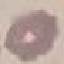
Result: negative for malaria parasites. Automatically extracted cell patch, resized to 64 × 64 pixels. Giemsa stain. Acquired by smartphone through the microscope eyepiece. Thin blood film.